Find each parasitized RBC.
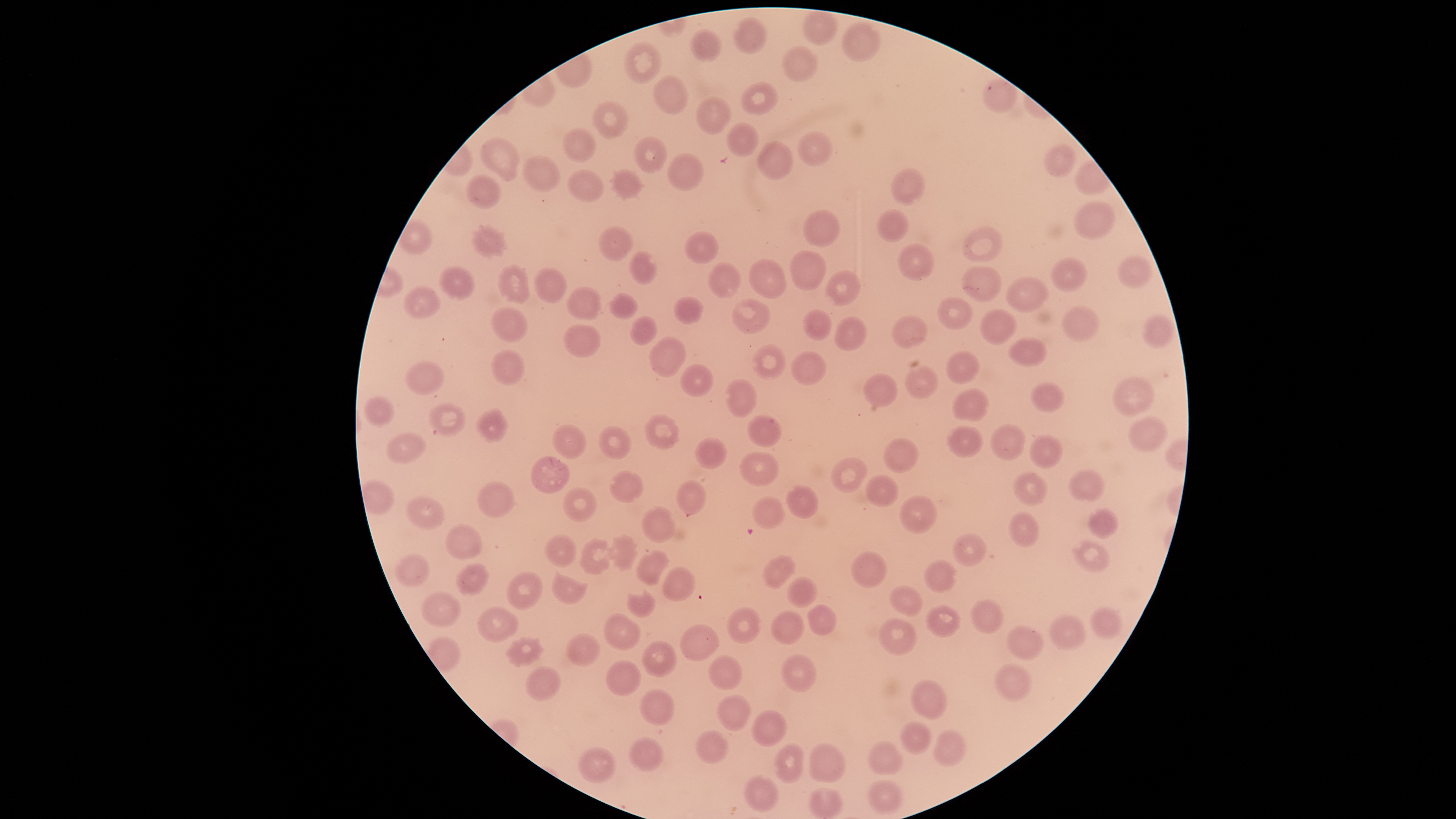

No parasitized RBCs identified.

{
  "field_of_view": "single",
  "stain": "Giemsa",
  "uninfected_RBCs": "approximate bounding boxes, in pixels from the top-left corner: (left=803, top=11, right=839, bottom=44), (left=735, top=18, right=767, bottom=54), (left=842, top=22, right=881, bottom=62), (left=690, top=30, right=723, bottom=63), (left=624, top=42, right=662, bottom=84), (left=782, top=46, right=819, bottom=82), (left=653, top=76, right=688, bottom=116), (left=983, top=77, right=1019, bottom=112), (left=741, top=82, right=778, bottom=115), (left=695, top=97, right=732, bottom=134), (left=594, top=101, right=629, bottom=138), (left=726, top=123, right=758, bottom=157), (left=562, top=128, right=596, bottom=163), (left=797, top=130, right=834, bottom=167), (left=633, top=136, right=667, bottom=172), (left=480, top=138, right=519, bottom=176), (left=757, top=141, right=794, bottom=180), (left=1044, top=144, right=1076, bottom=177), (left=667, top=153, right=702, bottom=190), (left=522, top=156, right=560, bottom=193), (left=892, top=168, right=925, bottom=205), (left=567, top=170, right=605, bottom=202), (left=612, top=170, right=642, bottom=198), (left=466, top=175, right=502, bottom=209), (left=1074, top=201, right=1115, bottom=239), (left=876, top=209, right=910, bottom=243), (left=803, top=210, right=840, bottom=247), (left=471, top=226, right=507, bottom=257), (left=598, top=226, right=633, bottom=260), (left=962, top=226, right=1003, bottom=262), (left=683, top=231, right=719, bottom=266), (left=897, top=243, right=935, bottom=282), (left=629, top=250, right=657, bottom=284), (left=790, top=251, right=827, bottom=291), (left=1119, top=255, right=1153, bottom=288), (left=1051, top=258, right=1087, bottom=292), (left=749, top=260, right=787, bottom=299), (left=709, top=262, right=741, bottom=298), (left=499, top=265, right=530, bottom=303), (left=439, top=266, right=476, bottom=298), (left=960, top=266, right=1002, bottom=303), (left=535, top=267, right=566, bottom=303), (left=825, top=271, right=861, bottom=307), (left=1006, top=276, right=1048, bottom=312), (left=404, top=286, right=440, bottom=318), (left=567, top=286, right=601, bottom=320), (left=610, top=293, right=638, bottom=318), (left=674, top=296, right=704, bottom=324), (left=937, top=296, right=973, bottom=330), (left=731, top=299, right=770, bottom=334), (left=1061, top=306, right=1100, bottom=343), (left=490, top=307, right=528, bottom=343), (left=802, top=309, right=832, bottom=340), (left=979, top=309, right=1017, bottom=345), (left=1142, top=314, right=1174, bottom=349), (left=631, top=315, right=658, bottom=346), (left=891, top=316, right=928, bottom=349), (left=834, top=317, right=866, bottom=350), (left=564, top=324, right=601, bottom=358), (left=650, top=337, right=686, bottom=376), (left=1007, top=338, right=1048, bottom=368), (left=753, top=345, right=787, bottom=381), (left=491, top=350, right=525, bottom=386), (left=791, top=351, right=827, bottom=386), (left=945, top=352, right=979, bottom=384), (left=405, top=362, right=444, bottom=395), (left=681, top=363, right=713, bottom=396), (left=904, top=366, right=939, bottom=400), (left=864, top=373, right=899, bottom=408), (left=1112, top=377, right=1155, bottom=416), (left=725, top=378, right=757, bottom=418), (left=1030, top=381, right=1064, bottom=412), (left=952, top=389, right=990, bottom=422), (left=363, top=396, right=395, bottom=427), (left=428, top=403, right=466, bottom=436), (left=475, top=409, right=508, bottom=442), (left=644, top=414, right=679, bottom=449), (left=746, top=414, right=781, bottom=447), (left=1128, top=416, right=1169, bottom=452), (left=990, top=423, right=1026, bottom=461), (left=552, top=424, right=588, bottom=459), (left=599, top=425, right=632, bottom=460), (left=947, top=426, right=983, bottom=458), (left=385, top=433, right=426, bottom=463), (left=1029, top=434, right=1062, bottom=468), (left=696, top=437, right=727, bottom=469), (left=883, top=438, right=919, bottom=473), (left=739, top=452, right=780, bottom=486), (left=531, top=456, right=568, bottom=493), (left=830, top=457, right=868, bottom=493), (left=1070, top=469, right=1105, bottom=501), (left=609, top=470, right=644, bottom=502), (left=1014, top=472, right=1049, bottom=507), (left=866, top=474, right=900, bottom=507), (left=676, top=480, right=706, bottom=515), (left=478, top=481, right=515, bottom=518), (left=785, top=485, right=820, bottom=518), (left=563, top=487, right=597, bottom=522), (left=753, top=495, right=783, bottom=529), (left=405, top=496, right=445, bottom=530), (left=899, top=496, right=937, bottom=533), (left=642, top=505, right=677, bottom=543), (left=1088, top=507, right=1118, bottom=538), (left=1010, top=510, right=1039, bottom=547), (left=445, top=524, right=482, bottom=560), (left=545, top=534, right=577, bottom=567), (left=953, top=534, right=986, bottom=566), (left=610, top=535, right=638, bottom=570), (left=580, top=540, right=610, bottom=575), (left=1072, top=540, right=1110, bottom=572), (left=636, top=549, right=671, bottom=586), (left=852, top=551, right=886, bottom=588), (left=395, top=552, right=430, bottom=588), (left=762, top=555, right=796, bottom=589), (left=923, top=559, right=955, bottom=591), (left=457, top=562, right=488, bottom=596), (left=663, top=566, right=696, bottom=602), (left=506, top=572, right=541, bottom=610), (left=551, top=572, right=588, bottom=605), (left=787, top=576, right=817, bottom=607), (left=890, top=586, right=922, bottom=616), (left=627, top=589, right=656, bottom=619), (left=422, top=591, right=461, bottom=626), (left=971, top=598, right=1003, bottom=634), (left=808, top=604, right=837, bottom=634), (left=925, top=604, right=961, bottom=637), (left=477, top=605, right=518, bottom=642), (left=726, top=606, right=762, bottom=643), (left=1092, top=606, right=1122, bottom=638), (left=771, top=610, right=805, bottom=645), (left=604, top=614, right=641, bottom=650), (left=1050, top=614, right=1086, bottom=649), (left=879, top=618, right=917, bottom=655), (left=680, top=624, right=719, bottom=661), (left=1007, top=626, right=1042, bottom=659), (left=568, top=633, right=599, bottom=666), (left=508, top=638, right=540, bottom=664), (left=642, top=641, right=677, bottom=677), (left=782, top=653, right=816, bottom=692), (left=708, top=655, right=742, bottom=689), (left=606, top=659, right=641, bottom=695), (left=995, top=663, right=1032, bottom=702), (left=526, top=666, right=560, bottom=701), (left=911, top=677, right=946, bottom=719), (left=641, top=689, right=674, bottom=726), (left=718, top=695, right=751, bottom=731), (left=752, top=709, right=788, bottom=747), (left=902, top=721, right=932, bottom=755), (left=697, top=731, right=728, bottom=763), (left=933, top=732, right=965, bottom=765), (left=629, top=737, right=664, bottom=773), (left=867, top=741, right=902, bottom=776), (left=810, top=743, right=845, bottom=782), (left=774, top=744, right=805, bottom=783), (left=578, top=746, right=615, bottom=785), (left=745, top=774, right=779, bottom=811), (left=867, top=778, right=904, bottom=814), (left=809, top=786, right=842, bottom=818)",
  "preparation": "thin smear of blood",
  "image_size": "1456×819 pixels",
  "capture": "smartphone photograph through the microscope eyepiece",
  "visible_region": "circular"
}